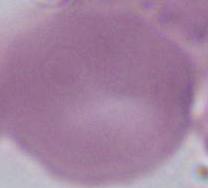

Summary:
  - Modality: micrograph
  - Magnification: 1000x
  - Identification: erythrocyte